Assess the morphology of the red blood cells.
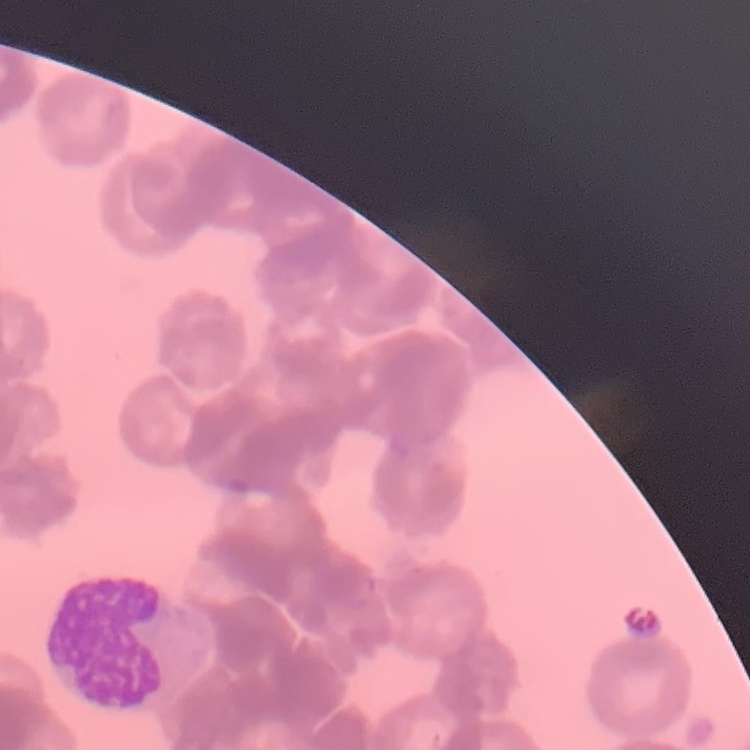
They show rouleaux formation.

preparation: thin blood smear
image_type: square crop of a larger photomicrograph
stain: Field's or Giemsa